Point out malaria parasites and leukocytes.
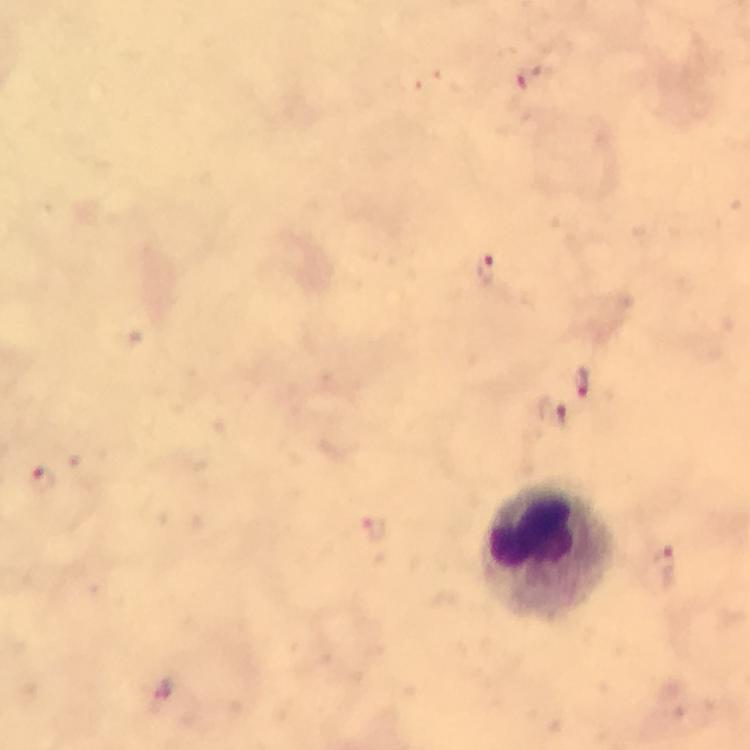
Approximate object centers, in pixels from the top-left corner.
Malaria parasites: (x=533, y=79), (x=486, y=269), (x=580, y=383), (x=551, y=410), (x=43, y=480), (x=374, y=529), (x=664, y=564).
Leukocytes: (x=542, y=551).

image size = 750×750 pixels
cropped from = a single field of view
stain = Giemsa
context = from a diagnostic examination for malaria
immersion oil = used
preparation = thick smear
capture = smartphone camera through the microscope
magnification = 100x